Classify this cell by malaria status.
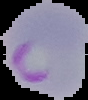

Parasitized.

Summary:
  - Image size: 88×100 pixels
  - Preparation: thin blood smear
  - Image type: segmented cell region on a black background